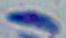

modality: micrograph
identification: Toxoplasma gondii
magnification: 1000x